Locate and identify every blood parasite.
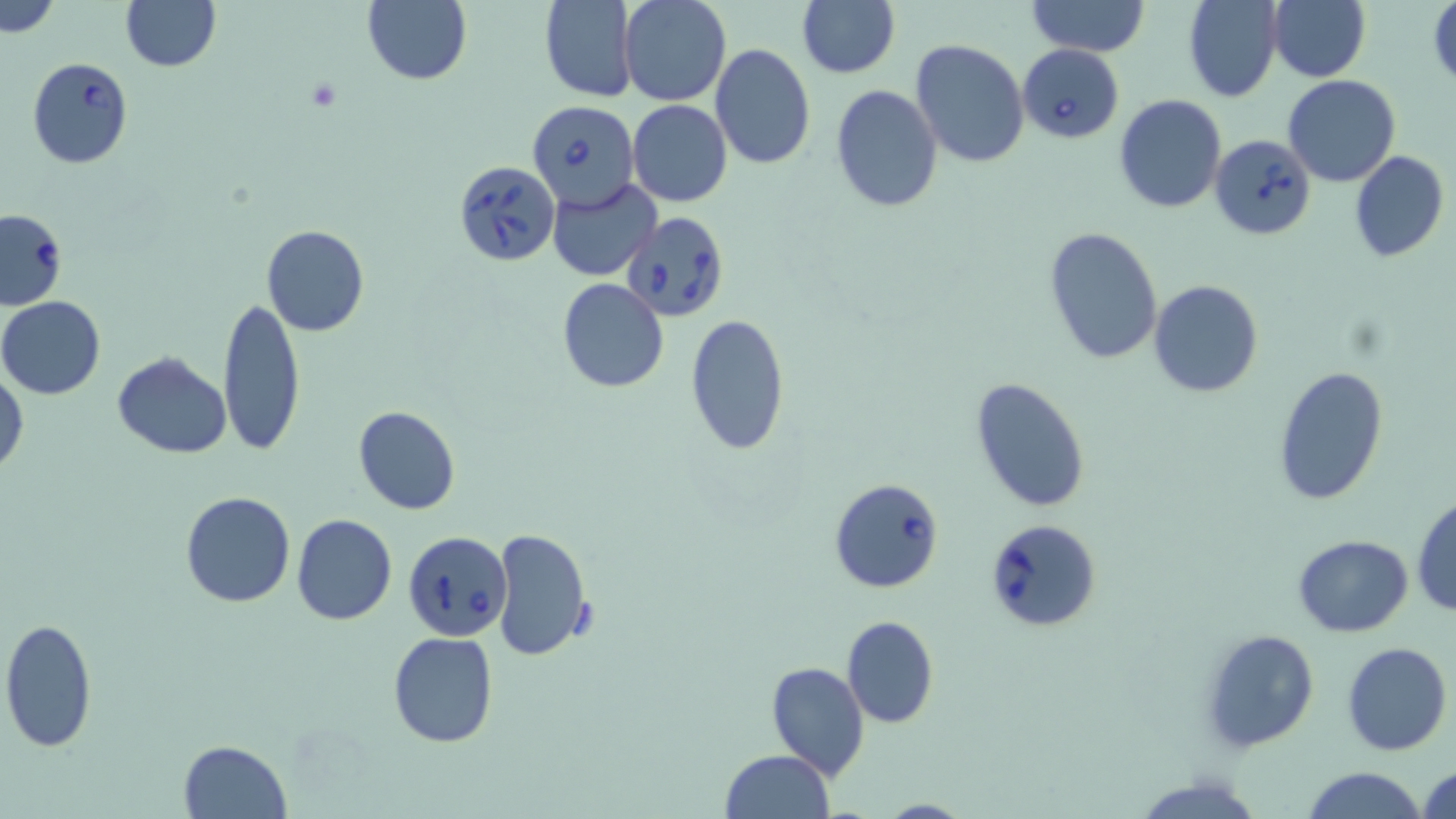

Approximate bounding boxes as named x1/y1/x2/y2 corners in pixels.
Babesia divergens-infected red blood cells: (x1=1017, y1=44, x2=1124, y2=144), (x1=26, y1=57, x2=133, y2=169), (x1=527, y1=99, x2=639, y2=212), (x1=1209, y1=134, x2=1317, y2=239), (x1=454, y1=159, x2=560, y2=266), (x1=0, y1=209, x2=68, y2=310), (x1=622, y1=213, x2=729, y2=324), (x1=829, y1=479, x2=944, y2=593), (x1=985, y1=518, x2=1103, y2=633), (x1=404, y1=531, x2=513, y2=642).
No Plasmodium falciparum, Plasmodium ovale, Plasmodium malariae, Plasmodium vivax, or Trypanosoma brucei observed.

Summary:
  - Platelet locations: (x1=305, y1=79, x2=339, y2=112)
  - Uninfected red blood cell locations: (x1=120, y1=0, x2=221, y2=72), (x1=539, y1=0, x2=639, y2=103), (x1=619, y1=0, x2=731, y2=105), (x1=1025, y1=0, x2=1149, y2=56), (x1=1182, y1=0, x2=1283, y2=103), (x1=1268, y1=0, x2=1370, y2=83), (x1=1427, y1=0, x2=1456, y2=89), (x1=0, y1=1, x2=62, y2=38), (x1=361, y1=1, x2=472, y2=85), (x1=796, y1=1, x2=899, y2=77), (x1=910, y1=39, x2=1030, y2=169), (x1=710, y1=42, x2=815, y2=170), (x1=1283, y1=74, x2=1401, y2=187), (x1=830, y1=84, x2=942, y2=211), (x1=1113, y1=94, x2=1227, y2=215), (x1=628, y1=101, x2=732, y2=207), (x1=1349, y1=150, x2=1450, y2=263), (x1=546, y1=180, x2=662, y2=280), (x1=260, y1=224, x2=369, y2=337), (x1=1043, y1=226, x2=1163, y2=364), (x1=558, y1=278, x2=669, y2=393), (x1=1150, y1=281, x2=1263, y2=400), (x1=217, y1=294, x2=305, y2=458), (x1=1, y1=296, x2=107, y2=400), (x1=684, y1=314, x2=791, y2=456), (x1=112, y1=353, x2=232, y2=458), (x1=1272, y1=365, x2=1390, y2=509), (x1=0, y1=373, x2=27, y2=477), (x1=970, y1=376, x2=1092, y2=512), (x1=354, y1=406, x2=460, y2=515), (x1=179, y1=491, x2=297, y2=608), (x1=1411, y1=496, x2=1456, y2=618), (x1=291, y1=513, x2=399, y2=626), (x1=490, y1=528, x2=594, y2=662), (x1=1294, y1=534, x2=1413, y2=636), (x1=842, y1=615, x2=938, y2=728), (x1=1, y1=619, x2=97, y2=753), (x1=1199, y1=628, x2=1320, y2=753), (x1=388, y1=632, x2=498, y2=748), (x1=1341, y1=641, x2=1451, y2=755), (x1=766, y1=661, x2=870, y2=780), (x1=178, y1=739, x2=291, y2=819), (x1=721, y1=749, x2=834, y2=819), (x1=1417, y1=763, x2=1456, y2=819), (x1=1300, y1=767, x2=1430, y2=819), (x1=1130, y1=772, x2=1262, y2=819), (x1=872, y1=798, x2=973, y2=818)
  - Slide-level diagnosis: Babesia divergens
  - Preparation: thin blood smear
  - Image size: 1456×819 pixels
  - Magnification: 1000x
  - Modality: light microscopy
  - Field of view: one of a larger specimen
  - Stain: May-Grünwald-Giemsa